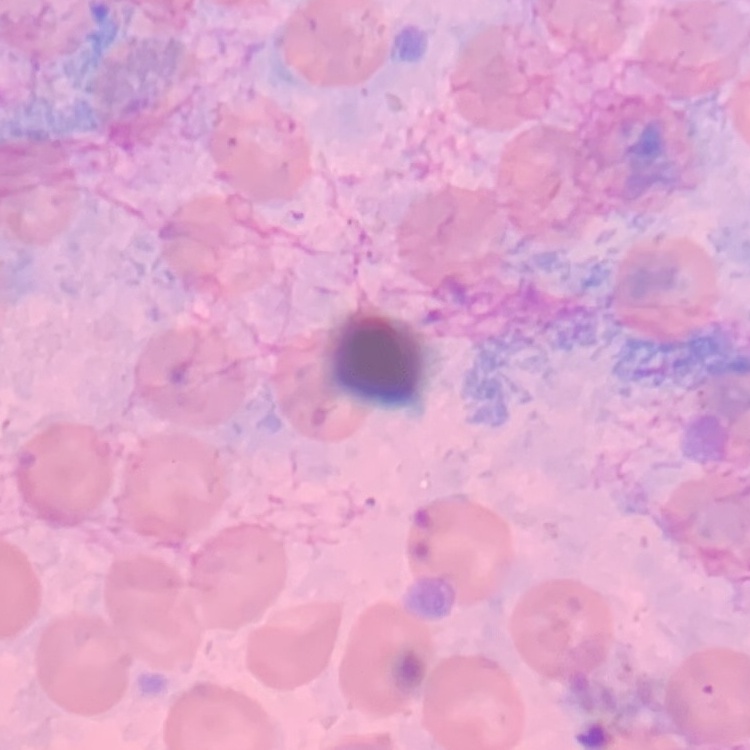

Summary:
  - Erythrocyte morphology: no rouleaux formation
  - Stain: Field's or Giemsa
  - Preparation: thin blood smear
  - Image type: square crop of a larger photomicrograph